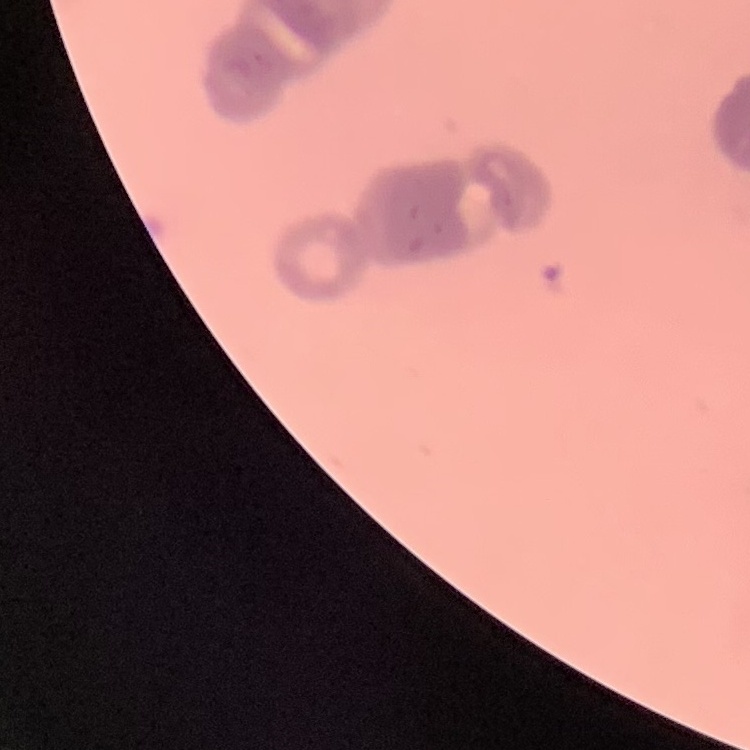

Summary:
  - Erythrocyte morphology: rouleaux formation
  - Stain: Field's or Giemsa
  - Preparation: thin peripheral smear
  - Image type: one tile cut from a larger photomicrograph